Comment on the morphology of the red blood cells.
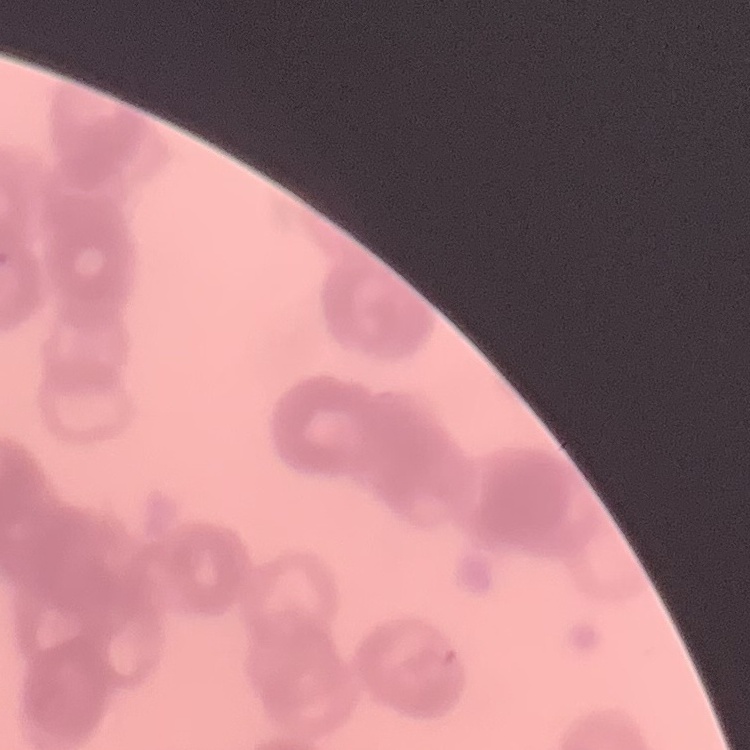

Rouleaux formation.

Summary:
  - Image type: square crop of a larger photomicrograph
  - Preparation: thin blood smear
  - Stain: Field's or Giemsa